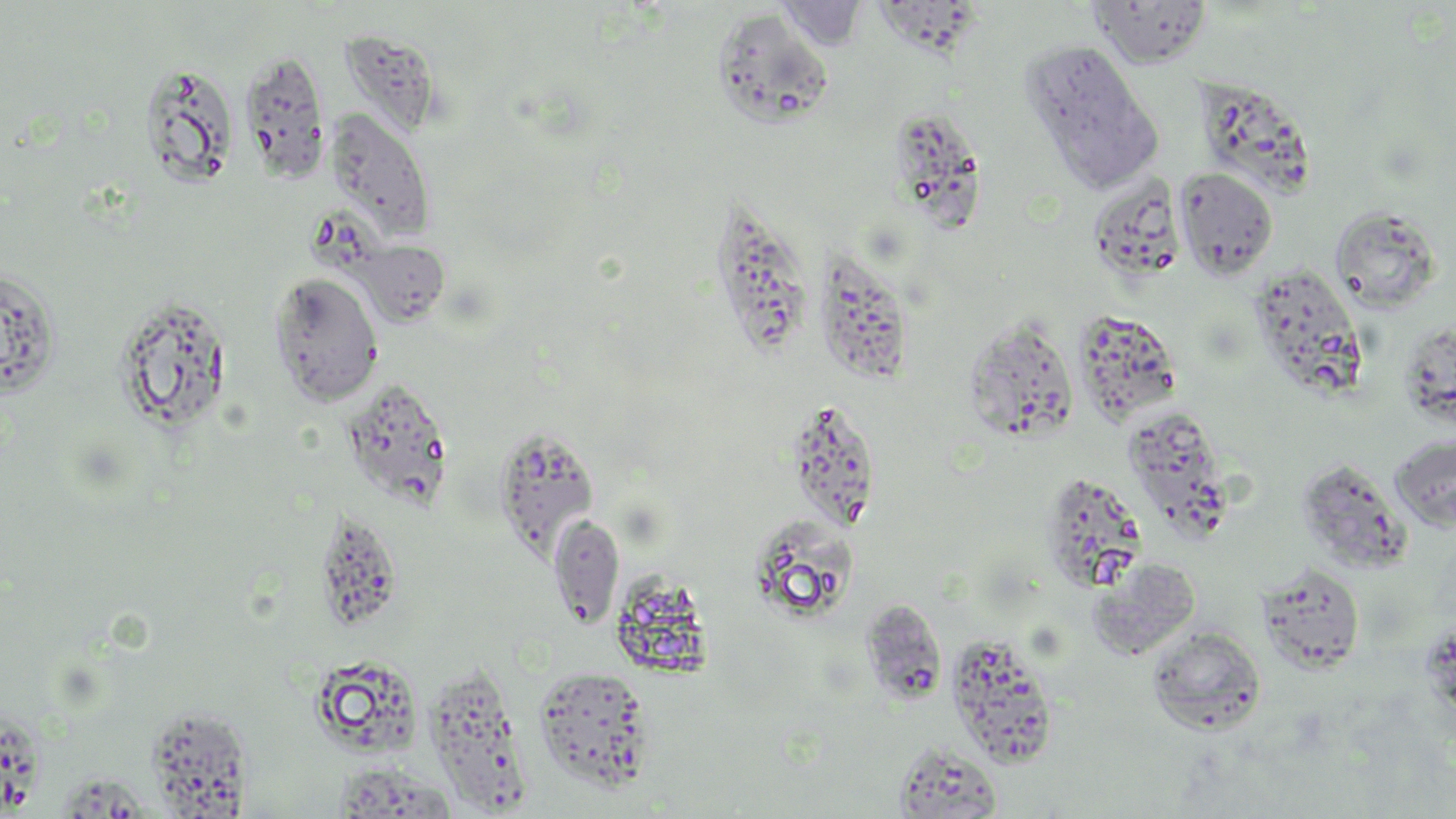

Approximate bounding boxes as [x1, y1, x2, y2] in pixels. Uninfected red blood cell locations: [776, 1, 869, 50], [1088, 1, 1214, 70], [879, 2, 988, 72], [712, 8, 836, 130], [339, 30, 434, 131], [1021, 40, 1163, 193], [239, 48, 332, 183], [140, 60, 240, 189], [1196, 81, 1314, 203], [324, 107, 436, 242], [900, 112, 985, 238], [1174, 166, 1279, 280], [1087, 176, 1185, 284], [704, 196, 804, 356], [1330, 206, 1442, 313], [349, 239, 451, 328], [811, 249, 916, 386], [1248, 265, 1366, 396], [0, 267, 60, 399], [268, 272, 385, 407], [113, 296, 233, 433], [1073, 311, 1182, 426], [963, 315, 1079, 443], [1399, 322, 1455, 427], [343, 381, 456, 510], [790, 403, 873, 533], [1122, 406, 1233, 529], [491, 427, 599, 557], [1389, 432, 1456, 533], [1296, 458, 1413, 575], [1038, 472, 1148, 593], [313, 507, 403, 632], [549, 513, 624, 628], [748, 515, 862, 623], [1088, 559, 1202, 661], [1256, 563, 1366, 674], [860, 599, 948, 707], [1146, 625, 1267, 735], [956, 635, 1055, 773], [315, 659, 425, 763], [422, 664, 540, 817], [534, 666, 655, 792], [0, 704, 44, 819], [145, 707, 252, 815], [893, 742, 1003, 819], [326, 762, 454, 819], [58, 772, 151, 819]. Slide-level diagnosis: no evidence of blood parasites. Light microscopy. May-Grünwald-Giemsa stain. Image is 1456×819 pixels. Thin blood film. Captured at 1000x magnification. One field of a larger specimen.